Give the position of every Plasmodium parasite visible.
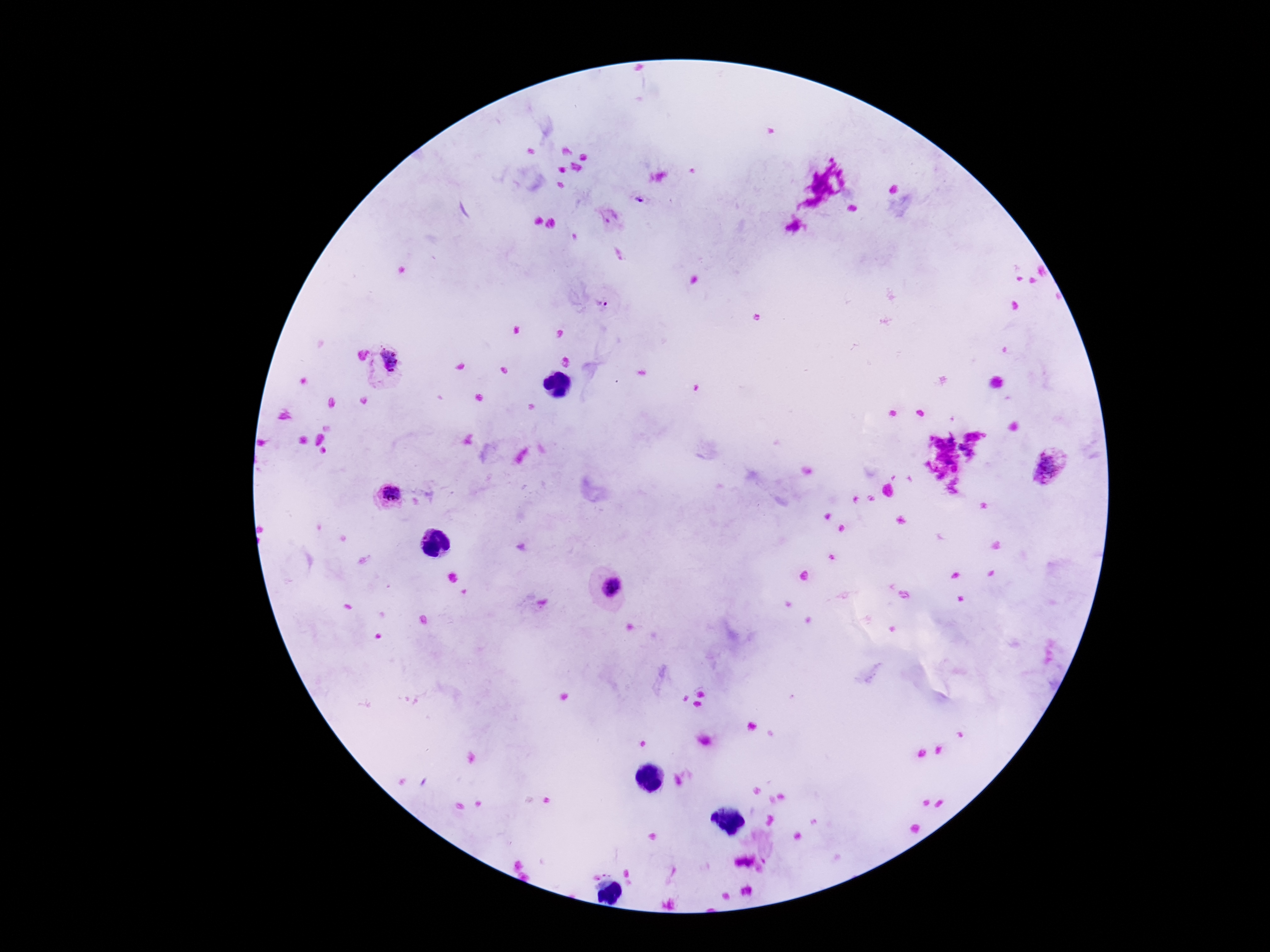

Approximate centers as (x, y) in pixels.
Plasmodium parasites: (639, 201), (610, 217), (603, 306), (386, 365), (1048, 468), (386, 494), (612, 588).

Summary:
  - Patient malaria status: positive
  - Preparation: thick peripheral-blood smear
  - Image size: 1270×952 pixels
  - Field of view: single
  - Stain: Giemsa
  - Magnification: 100x
  - Capture: smartphone camera through the microscope eyepiece